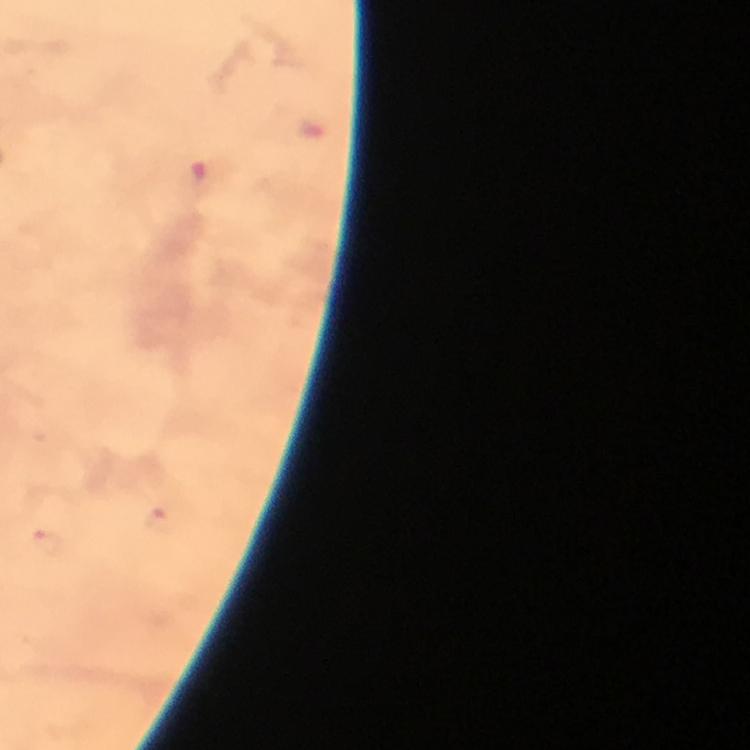
Approximate centers as {x, y} in pixels. Plasmodium parasite locations: {161, 521}, {49, 542}. Immersion oil was used. Thick smear. Photographed through the microscope with a smartphone camera. Giemsa stain. At 100x magnification. From a diagnostic examination for malaria. Image is 750×750 pixels. Cropped region of a single field of view.